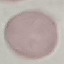
Malaria status: uninfected. Giemsa-stained preparation. Acquired by smartphone through the microscope eyepiece. Cell patch, automatically extracted from a larger field of view and resized to 64 × 64 pixels. Thin blood film.